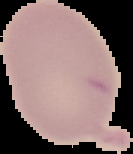

From a thin blood film. The area outside the segmented cell region is set to black. Image is 133×154 pixels. Result: no Plasmodium parasites detected.